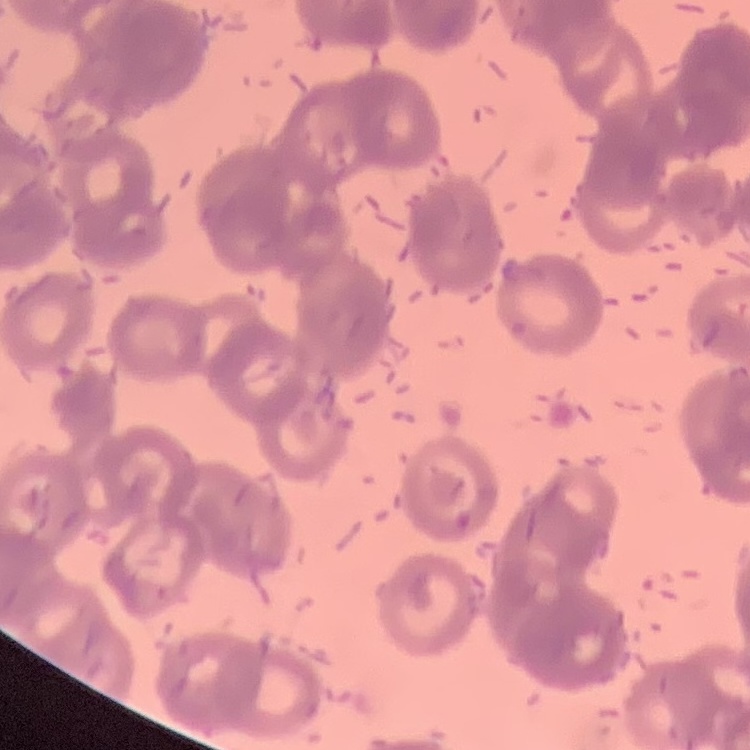

red blood cell morphology = rouleaux formation
preparation = thin blood smear
stain = Field's or Giemsa
image type = square crop of a larger photomicrograph